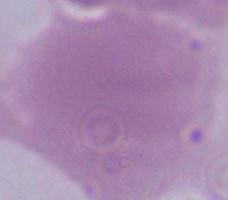

identification = erythrocyte
magnification = 1000x
modality = photomicrograph